Assess the morphology of the red blood cells.
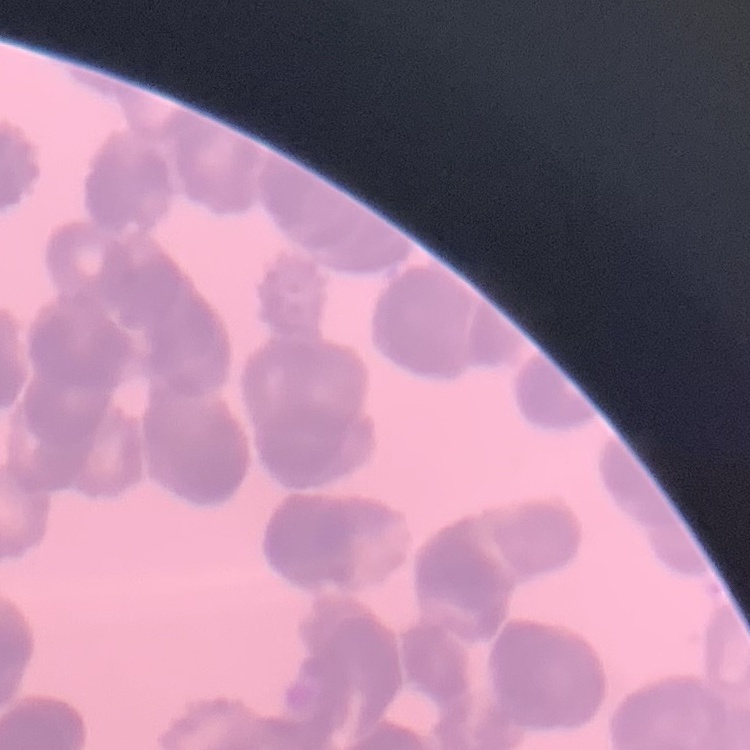

They show rouleaux formation.

Summary:
  - Stain: Field's or Giemsa
  - Image type: square crop of a larger photomicrograph
  - Preparation: thin peripheral smear